Assess this cell for malaria.
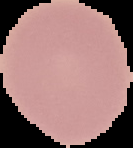
Uninfected.

From a thin blood smear. Image is 133×148 pixels. Segmented cell region on a black background.